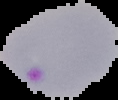

Summary:
  - Image type: segmented cell region on a black background
  - Image size: 118×100 pixels
  - Preparation: thin blood smear
  - Malaria status: parasitized